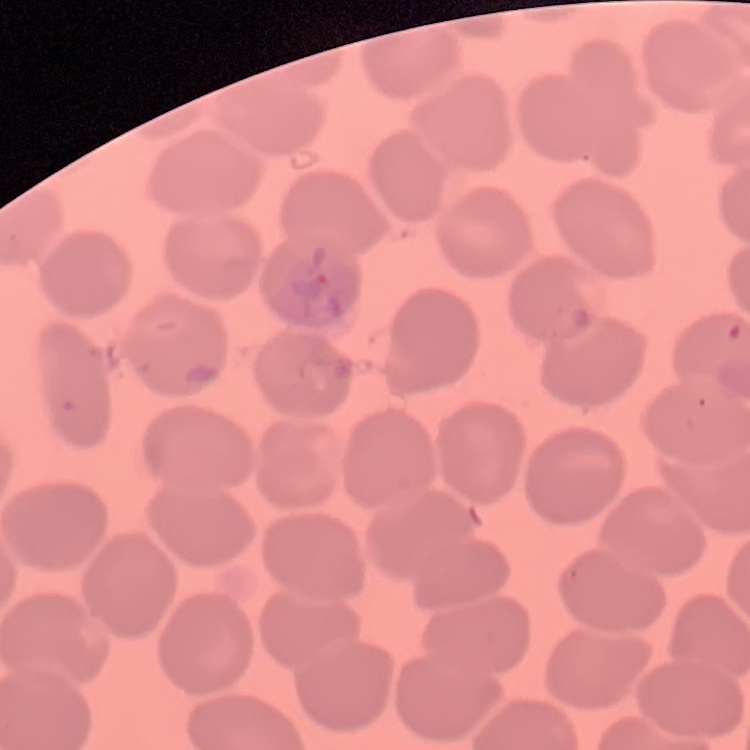 The erythrocytes show no rouleaux formation. Thin peripheral smear. Stained with either Field's or Giemsa. One tile cut from a larger photomicrograph.